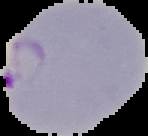
image_size: 148×136 pixels
image_type: cell region segmented out of the field of view; surrounding area masked to black
preparation: thin blood film
result: malaria parasites identified